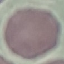
malaria_status: uninfected
stain: Giemsa
image_type: automatically extracted cell patch, resized to 64 × 64 pixels
preparation: thin smear
capture: smartphone through the microscope eyepiece